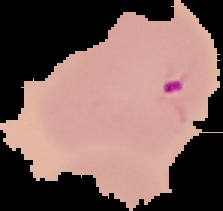

Summary:
  - Malaria status: parasitized
  - Preparation: thin blood smear
  - Image size: 223×211 pixels
  - Image type: segmented cell region on a black background